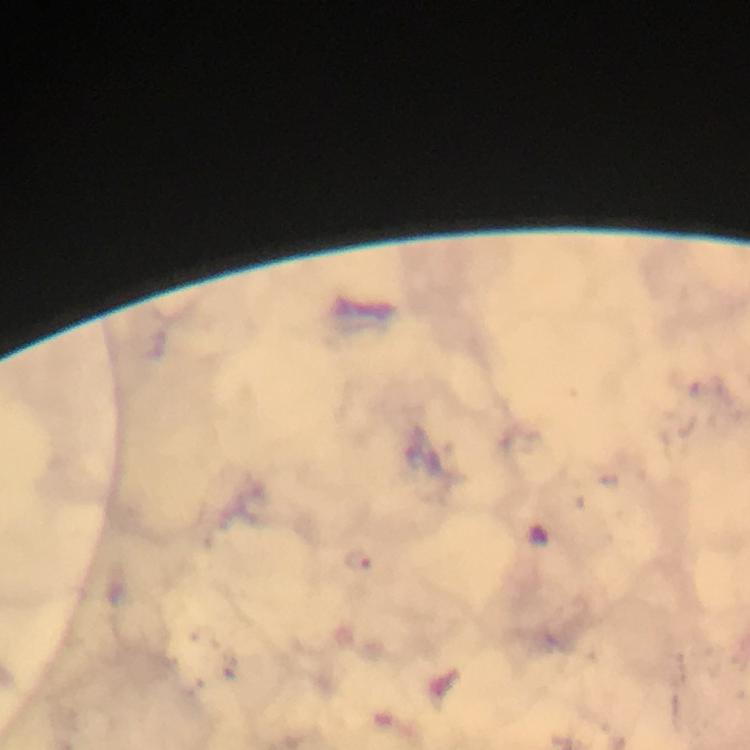

{
  "immersion_oil": "used",
  "preparation": "thick blood smear",
  "context": "from a malaria diagnostic workup",
  "capture": "smartphone camera through the microscope",
  "stain": "Giemsa",
  "cropped_from": "a single field of view",
  "image_size": "750×750 pixels",
  "malaria_parasite_locations": "approximate centers as {x, y} in pixels: {358, 557}",
  "magnification": "100x"
}